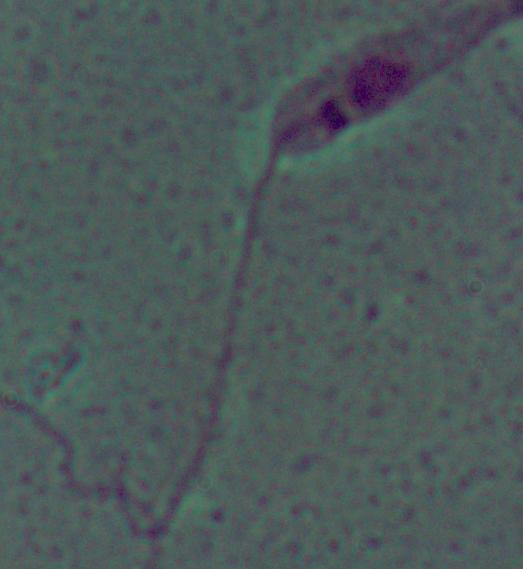
Photomicrograph. 1000x magnification. A Leishmania parasite is seen.